Outline each blood parasite and name the species.
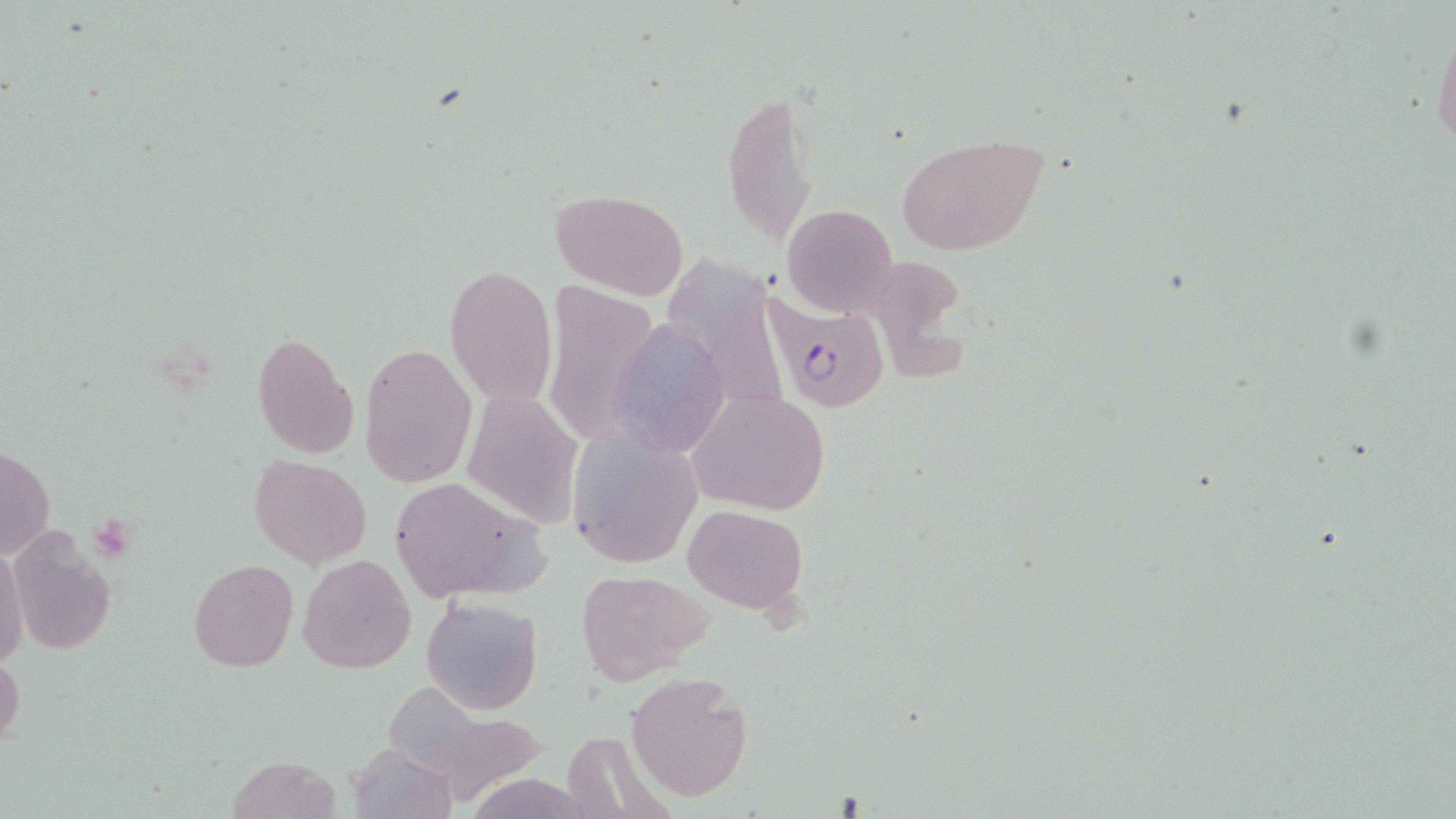

Approximate bounding boxes as (x1, y1, x2, y2) in pixels.
Plasmodium falciparum-infected red blood cells: (760, 295, 892, 414).
No Plasmodium ovale, Plasmodium malariae, Plasmodium vivax, Babesia divergens, or Trypanosoma brucei observed.

slide-level diagnosis = Plasmodium falciparum
platelet locations = approximate bounding boxes as (x1, y1, x2, y2) in pixels: (89, 515, 136, 560)
stain = May-Grünwald-Giemsa
uninfected red blood cell locations = approximate bounding boxes as (x1, y1, x2, y2) in pixels: (1430, 11, 1456, 155), (721, 87, 819, 246), (897, 133, 1049, 257), (549, 188, 691, 299), (782, 204, 897, 318), (878, 253, 979, 389), (661, 260, 778, 410), (445, 265, 557, 407), (541, 280, 660, 450), (605, 318, 730, 457), (250, 333, 360, 458), (359, 342, 477, 488), (687, 389, 830, 515), (460, 390, 584, 529), (568, 428, 701, 568), (1, 444, 55, 563), (250, 455, 371, 569), (387, 475, 549, 604), (684, 504, 805, 614), (5, 529, 116, 657), (1, 540, 28, 673), (299, 554, 417, 673), (189, 558, 298, 671), (576, 569, 714, 684), (422, 596, 543, 714), (0, 652, 25, 750), (625, 670, 756, 803), (391, 690, 547, 804), (559, 731, 676, 818), (348, 742, 457, 819), (225, 755, 344, 818)
image size = 1456×819 pixels
magnification = 1000x
modality = light microscopy
preparation = thin blood smear
field of view = single